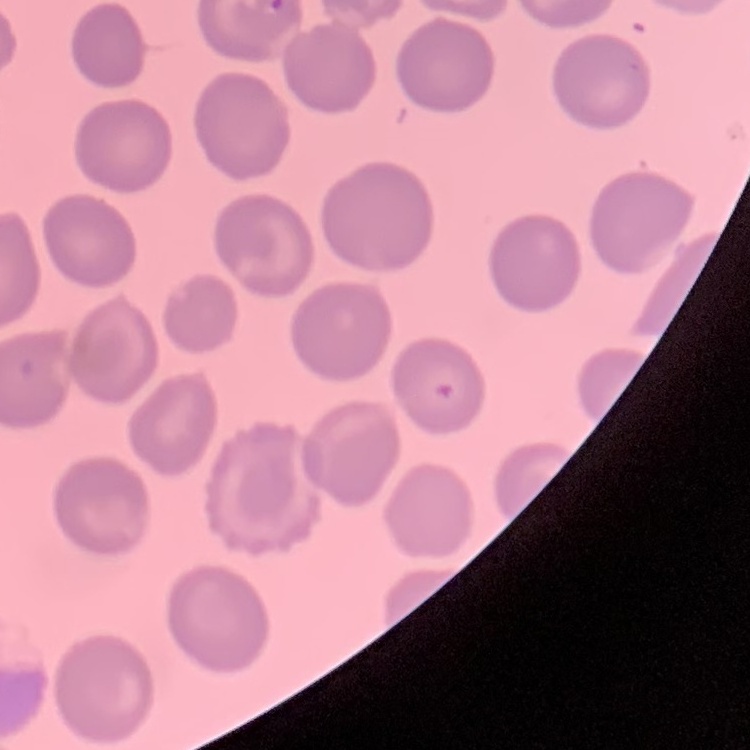

Summary:
  - Erythrocyte morphology: no rouleaux formation
  - Stain: Field's or Giemsa
  - Image type: square crop of a larger photomicrograph
  - Preparation: thin blood film